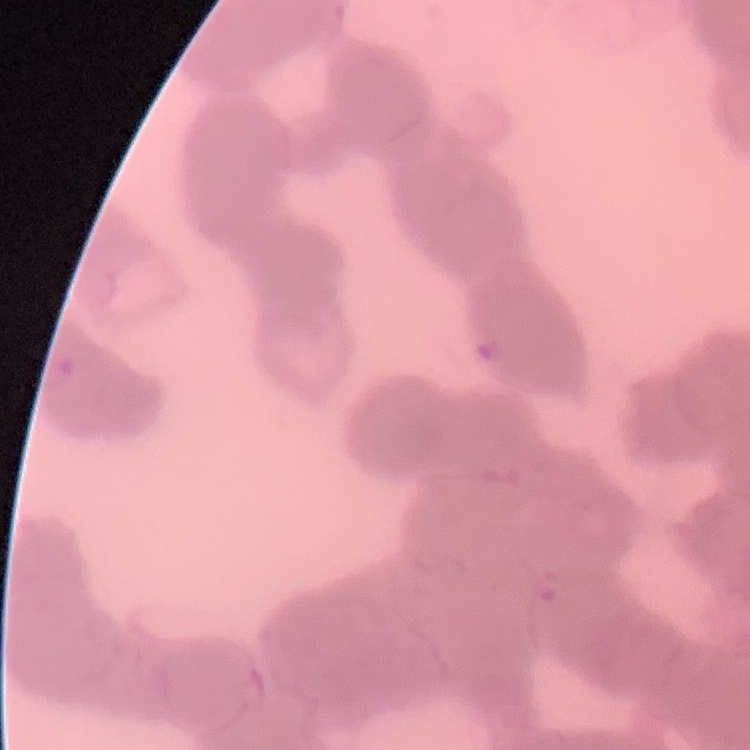

red blood cell morphology = rouleaux formation
stain = Field's or Giemsa
preparation = thin blood smear
image type = square crop of a larger photomicrograph